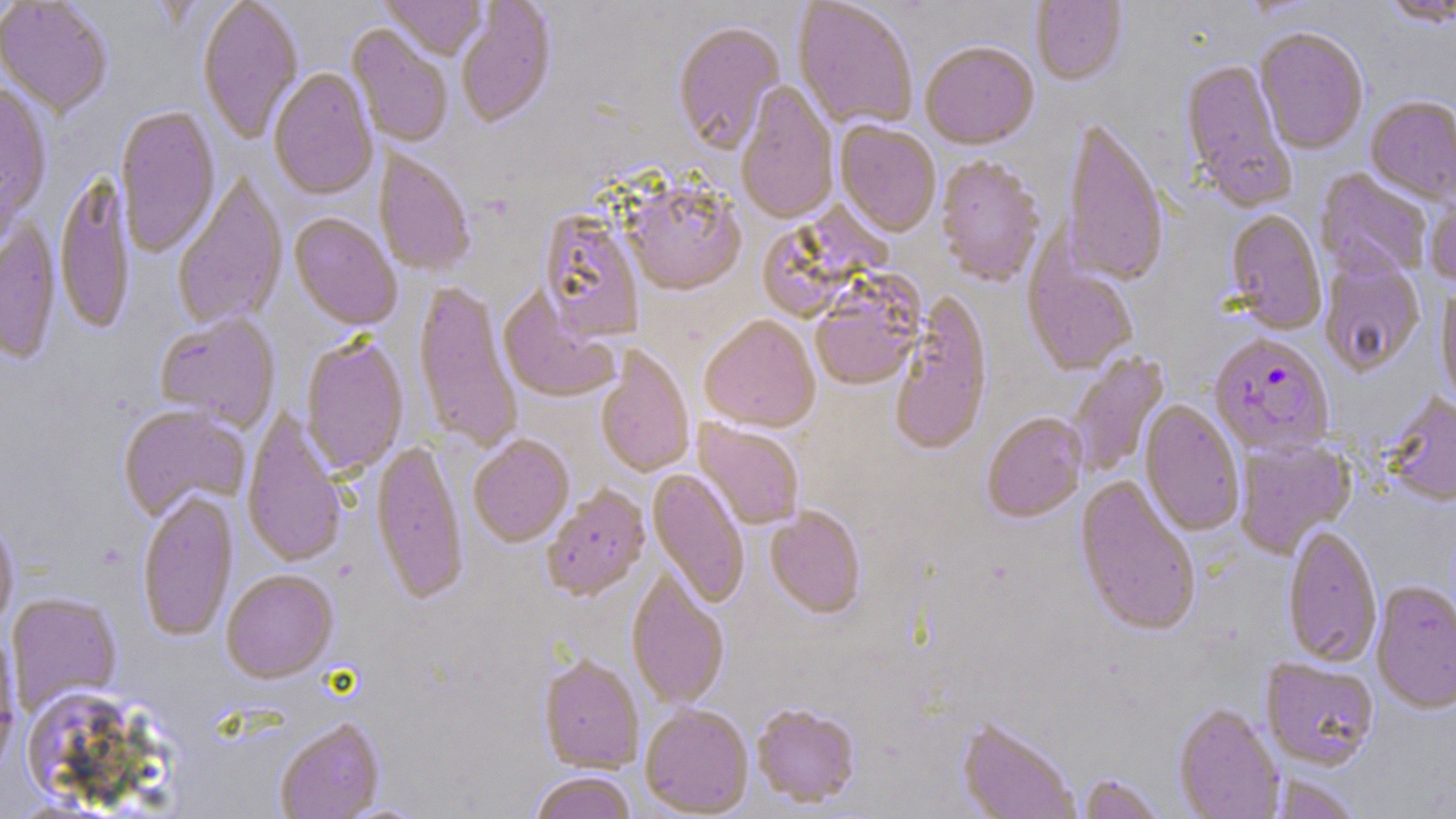
Approximate bounding boxes as named x1/y1/x2/y2 corners in pixels. Uninfected red blood cell locations: (x1=197, y1=0, x2=304, y2=145), (x1=379, y1=0, x2=487, y2=61), (x1=1031, y1=0, x2=1126, y2=87), (x1=1379, y1=0, x2=1456, y2=28), (x1=0, y1=1, x2=113, y2=117), (x1=456, y1=1, x2=557, y2=130), (x1=793, y1=1, x2=918, y2=132), (x1=672, y1=22, x2=786, y2=156), (x1=347, y1=25, x2=453, y2=149), (x1=1255, y1=30, x2=1368, y2=155), (x1=920, y1=44, x2=1039, y2=152), (x1=1179, y1=60, x2=1296, y2=211), (x1=268, y1=70, x2=378, y2=201), (x1=0, y1=81, x2=52, y2=232), (x1=736, y1=81, x2=838, y2=226), (x1=1365, y1=97, x2=1456, y2=207), (x1=115, y1=105, x2=221, y2=257), (x1=1061, y1=120, x2=1168, y2=289), (x1=835, y1=122, x2=941, y2=238), (x1=374, y1=147, x2=475, y2=278), (x1=936, y1=158, x2=1045, y2=288), (x1=1315, y1=168, x2=1432, y2=280), (x1=54, y1=171, x2=136, y2=336), (x1=172, y1=173, x2=288, y2=331), (x1=625, y1=184, x2=746, y2=297), (x1=1425, y1=186, x2=1456, y2=292), (x1=759, y1=200, x2=896, y2=322), (x1=539, y1=210, x2=645, y2=344), (x1=1225, y1=211, x2=1326, y2=335), (x1=289, y1=214, x2=402, y2=331), (x1=0, y1=219, x2=61, y2=366), (x1=1023, y1=250, x2=1138, y2=378), (x1=1320, y1=256, x2=1425, y2=379), (x1=412, y1=280, x2=522, y2=454), (x1=811, y1=283, x2=923, y2=391), (x1=1436, y1=286, x2=1456, y2=412), (x1=498, y1=287, x2=622, y2=404), (x1=889, y1=294, x2=992, y2=457), (x1=155, y1=313, x2=281, y2=432), (x1=699, y1=317, x2=820, y2=434), (x1=301, y1=335, x2=409, y2=477), (x1=596, y1=346, x2=694, y2=479), (x1=1068, y1=352, x2=1170, y2=477), (x1=1382, y1=393, x2=1456, y2=509), (x1=1139, y1=401, x2=1244, y2=537), (x1=118, y1=405, x2=249, y2=521), (x1=241, y1=407, x2=349, y2=570), (x1=982, y1=414, x2=1088, y2=524), (x1=693, y1=420, x2=804, y2=530), (x1=468, y1=437, x2=574, y2=548), (x1=1234, y1=438, x2=1357, y2=559), (x1=371, y1=440, x2=469, y2=606), (x1=647, y1=469, x2=749, y2=609), (x1=1074, y1=474, x2=1201, y2=640), (x1=543, y1=486, x2=650, y2=602), (x1=137, y1=490, x2=238, y2=642), (x1=765, y1=508, x2=866, y2=619), (x1=0, y1=512, x2=19, y2=632), (x1=1282, y1=527, x2=1382, y2=668), (x1=626, y1=568, x2=730, y2=711), (x1=221, y1=570, x2=339, y2=684), (x1=1370, y1=582, x2=1456, y2=716), (x1=7, y1=593, x2=122, y2=716), (x1=0, y1=632, x2=21, y2=776), (x1=539, y1=655, x2=644, y2=773), (x1=1261, y1=660, x2=1379, y2=772), (x1=21, y1=686, x2=151, y2=804), (x1=751, y1=704, x2=860, y2=809), (x1=1173, y1=704, x2=1285, y2=819), (x1=640, y1=705, x2=753, y2=817), (x1=957, y1=717, x2=1080, y2=819), (x1=275, y1=719, x2=385, y2=819), (x1=529, y1=773, x2=636, y2=819), (x1=1077, y1=774, x2=1166, y2=818), (x1=1267, y1=775, x2=1365, y2=819). Plasmodium falciparum-infected red blood cell locations: (x1=1209, y1=335, x2=1334, y2=459). Slide-level diagnosis: Plasmodium falciparum. Thin blood smear. Image is 1456×819 pixels. Optical microscopy. May-Grünwald-Giemsa-stained preparation. 1000x magnification. One field of a larger specimen.